Describe the morphology of the red blood cells.
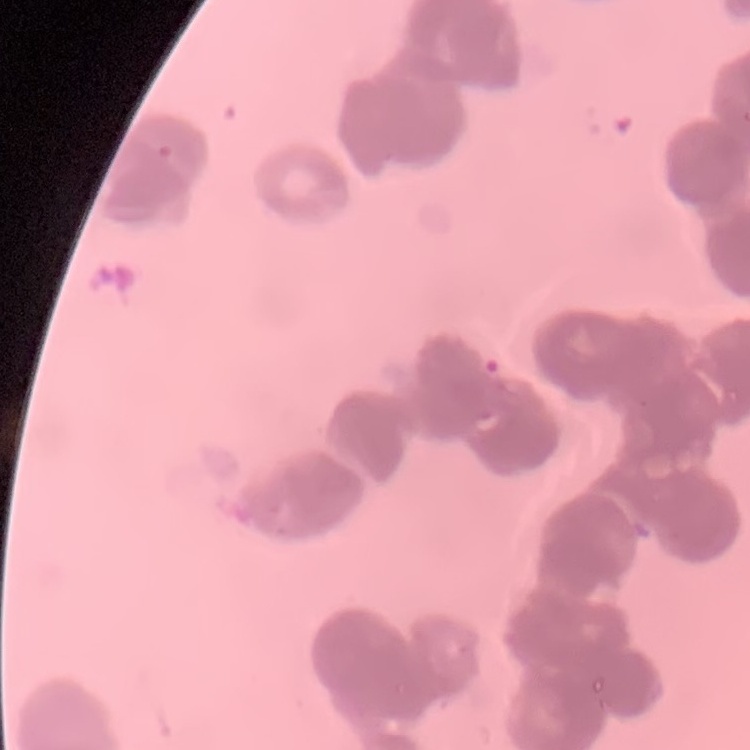
They show rouleaux formation.

Stained with either Field's or Giemsa. Thin peripheral smear. One tile cut from a larger photomicrograph.